Assess the morphology of the red blood cells.
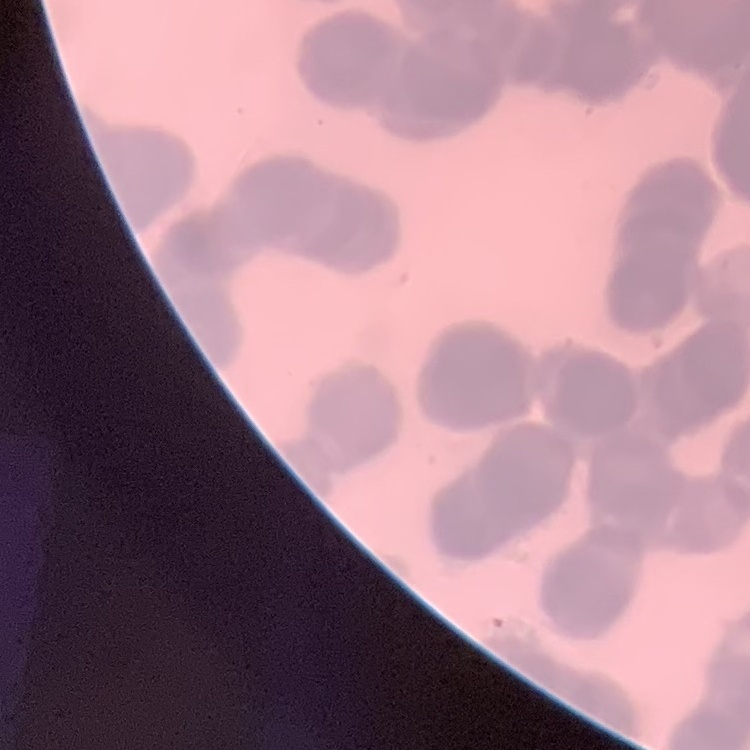
They show rouleaux formation.

Summary:
  - Image type: one tile cut from a larger photomicrograph
  - Stain: Field's or Giemsa
  - Preparation: thin peripheral smear